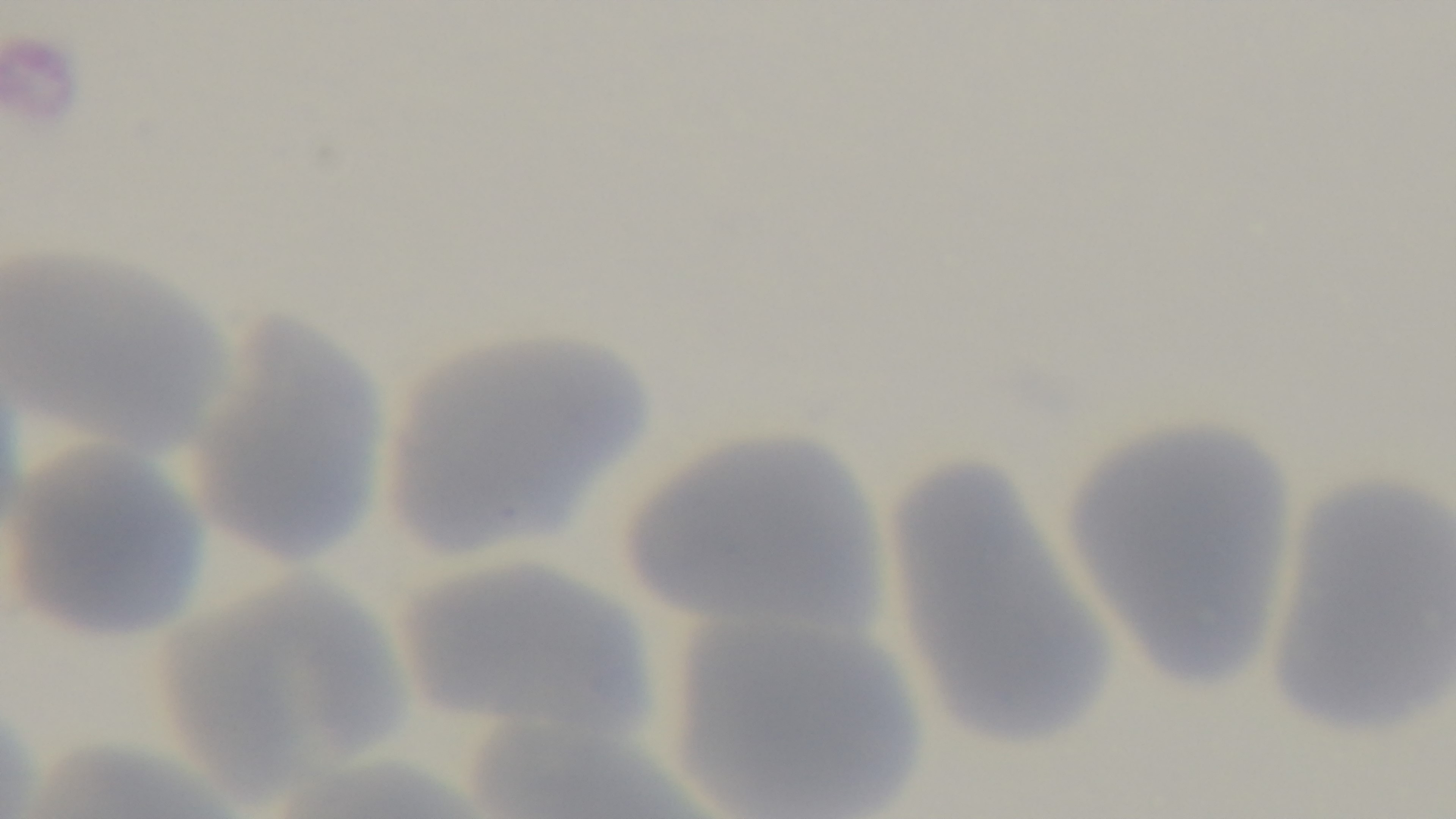
Summary:
  - Capture: mounted 4K digital camera
  - Objective: 100x oil immersion
  - Malaria status: negative
  - Modality: light microscopy
  - Field of view: one from the slide
  - Stain: Giemsa
  - Preparation: thin smear